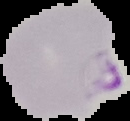
Summary:
  - Result: Plasmodium parasites identified
  - Preparation: thin blood smear
  - Image size: 130×121 pixels
  - Image type: cell region segmented out of the field of view; surrounding area masked to black